Give the position of every Plasmodium parasite visible.
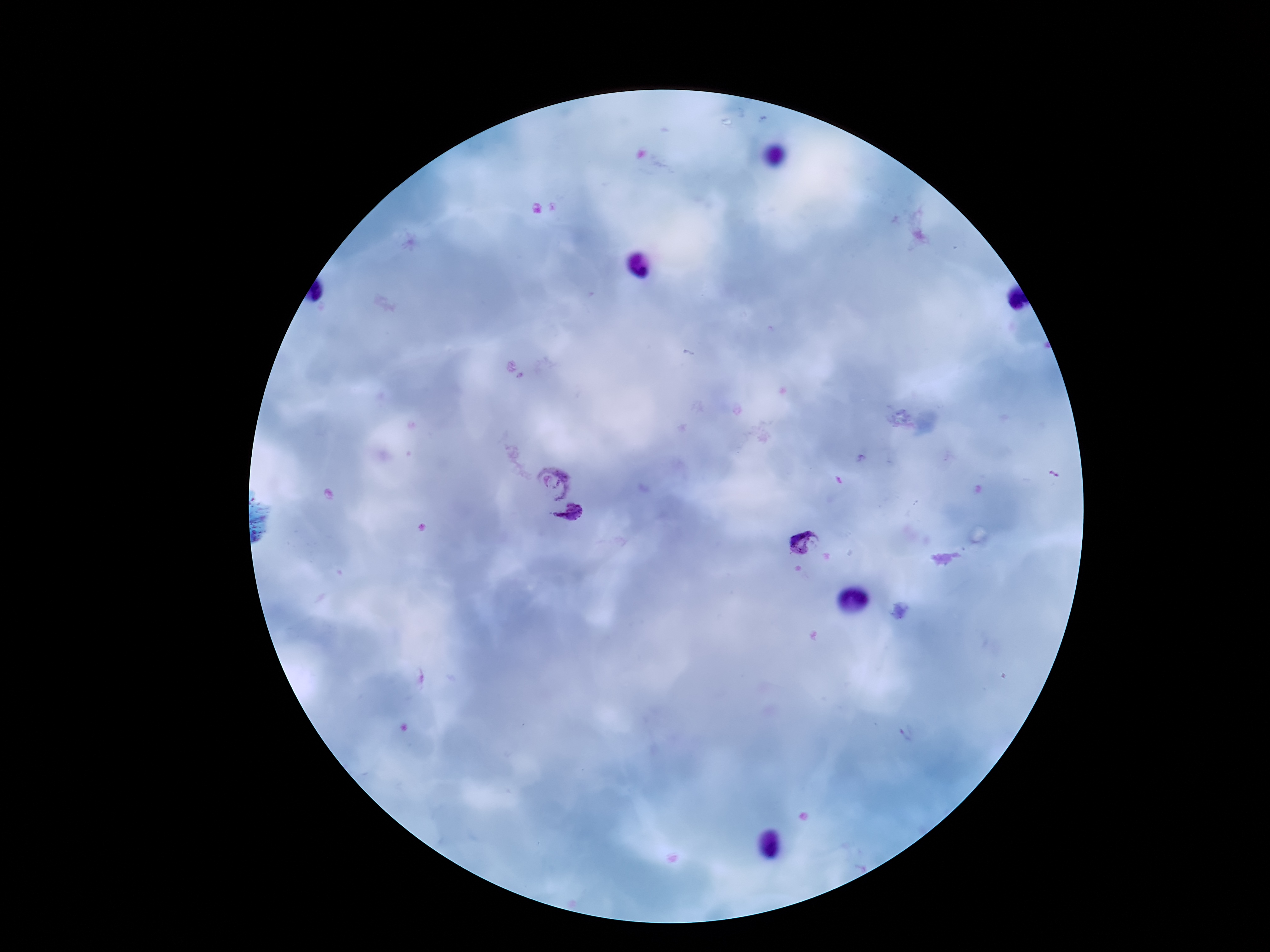
Approximate centers as (x, y) in pixels.
Plasmodium parasites: (552, 482), (569, 518), (804, 541).

Summary:
  - Image size: 1270×952 pixels
  - Field of view: one from this slide
  - Magnification: 100x
  - Preparation: thick peripheral-blood smear
  - Patient malaria status: infected
  - Stain: Giemsa
  - Capture: smartphone camera through the microscope eyepiece